Locate every blood parasite and identify its species.
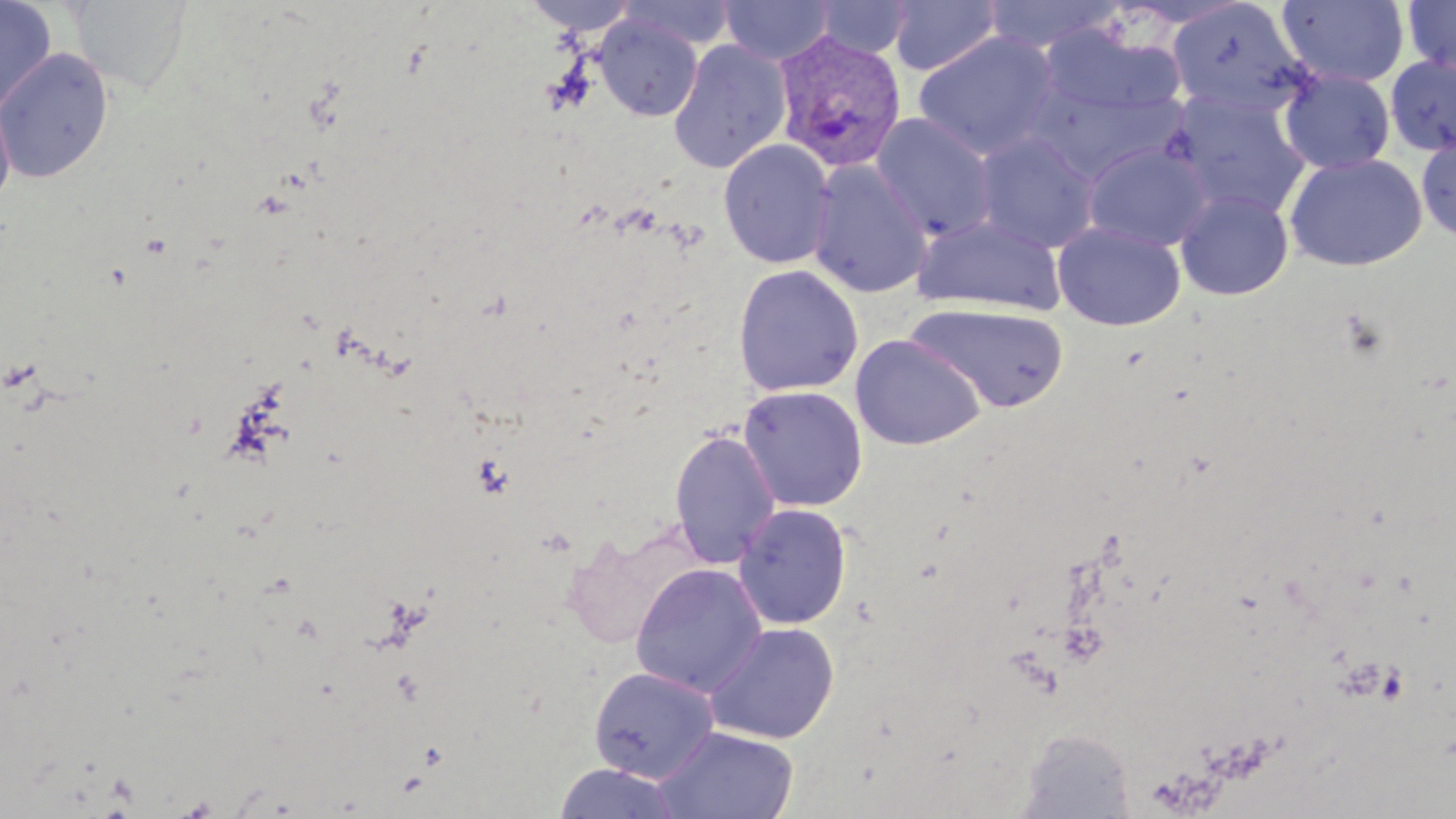
Approximate bounding boxes as (x1, y1, x2, y2) in pixels.
Plasmodium vivax-infected red blood cells: (773, 31, 908, 173).
No Plasmodium falciparum, Plasmodium ovale, Plasmodium malariae, Babesia divergens, or Trypanosoma brucei observed.

slide-level diagnosis = Plasmodium vivax
preparation = thin blood smear
magnification = 1000x
image size = 1456×819 pixels
uninfected red blood cell locations = approximate bounding boxes as (x1, y1, x2, y2) in pixels: (0, 0, 57, 115), (68, 0, 194, 96), (523, 0, 639, 36), (617, 0, 736, 50), (718, 0, 835, 65), (813, 0, 913, 59), (980, 0, 1124, 53), (1277, 0, 1409, 88), (1402, 0, 1456, 77), (887, 1, 1003, 76), (1166, 1, 1312, 120), (594, 14, 703, 122), (1039, 24, 1185, 122), (913, 32, 1060, 160), (668, 39, 792, 174), (1, 47, 113, 184), (1384, 55, 1456, 157), (1279, 68, 1396, 174), (1025, 78, 1183, 184), (0, 91, 17, 213), (1163, 91, 1312, 218), (870, 112, 998, 241), (1416, 130, 1456, 243), (972, 131, 1100, 253), (718, 139, 835, 269), (1081, 141, 1213, 252), (1283, 152, 1428, 271), (807, 160, 933, 298), (1175, 188, 1294, 300), (913, 213, 1066, 315), (1053, 222, 1186, 331), (731, 264, 864, 397), (907, 302, 1070, 414), (850, 334, 985, 451), (737, 385, 868, 512), (668, 428, 781, 569), (734, 503, 852, 630), (631, 563, 768, 698), (703, 622, 840, 744), (587, 665, 719, 783), (654, 726, 799, 818), (1017, 729, 1138, 817), (553, 763, 684, 819)
stain = May-Grünwald-Giemsa
field of view = one of a larger specimen
modality = optical microscopy